Locate and identify every blood parasite.
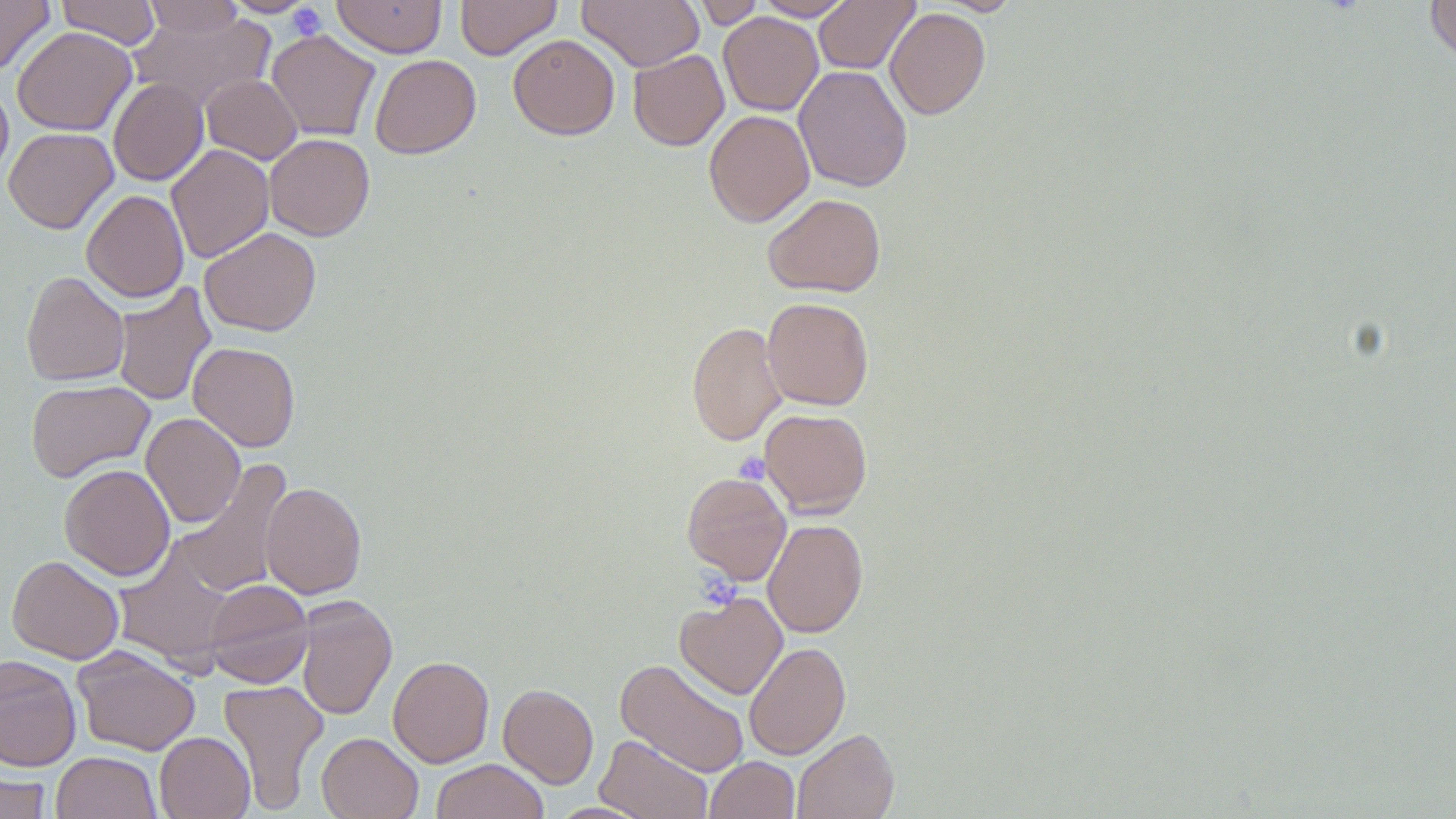
No blood parasites observed.

Summary:
  - Coordinate format: approximate bounding boxes as (x1,y1)-(x2,y2) corner pairs in pixels
  - Uninfected red blood cell locations: (0,0)-(55,76), (56,0)-(161,49), (221,0)-(318,17), (333,0)-(446,58), (455,0)-(561,60), (577,0)-(704,71), (691,0)-(765,28), (754,0)-(856,20), (814,0)-(919,74), (934,0)-(1023,15), (1425,0)-(1456,65), (141,1)-(245,39), (885,7)-(991,119), (128,11)-(275,113), (718,12)-(823,116), (12,26)-(136,136), (266,29)-(380,141), (508,34)-(619,140), (628,49)-(729,151), (370,54)-(481,159), (793,64)-(913,192), (201,74)-(302,164), (108,78)-(208,186), (0,79)-(13,183), (704,109)-(815,227), (3,127)-(118,233), (264,134)-(375,241), (166,144)-(274,263), (82,190)-(189,302), (763,193)-(886,297), (199,227)-(321,336), (21,271)-(130,386), (112,282)-(216,407), (762,297)-(874,410), (687,321)-(787,446), (188,341)-(301,452), (25,379)-(155,482), (759,407)-(872,518), (141,412)-(245,527), (172,460)-(292,598), (60,463)-(175,581), (682,471)-(792,585), (260,481)-(367,598), (763,518)-(868,638), (113,543)-(237,672), (6,555)-(124,665), (203,579)-(313,688), (675,592)-(788,699), (295,596)-(397,721), (744,641)-(851,760), (72,646)-(201,756), (0,655)-(82,772), (388,655)-(494,767), (615,657)-(750,778), (218,679)-(328,813), (498,683)-(598,789), (792,728)-(899,819), (155,731)-(255,819), (316,732)-(423,819), (595,734)-(713,819), (51,751)-(162,819), (704,756)-(800,819), (430,759)-(548,819), (0,770)-(52,819)
  - Platelet locations: (287,3)-(328,41), (734,451)-(770,484), (702,569)-(742,606)
  - Slide-level diagnosis: no evidence of blood parasites
  - Stain: May-Grünwald-Giemsa
  - Field of view: one of a larger specimen
  - Modality: optical microscopy
  - Preparation: thin blood smear
  - Magnification: 1000x
  - Image size: 1456×819 pixels